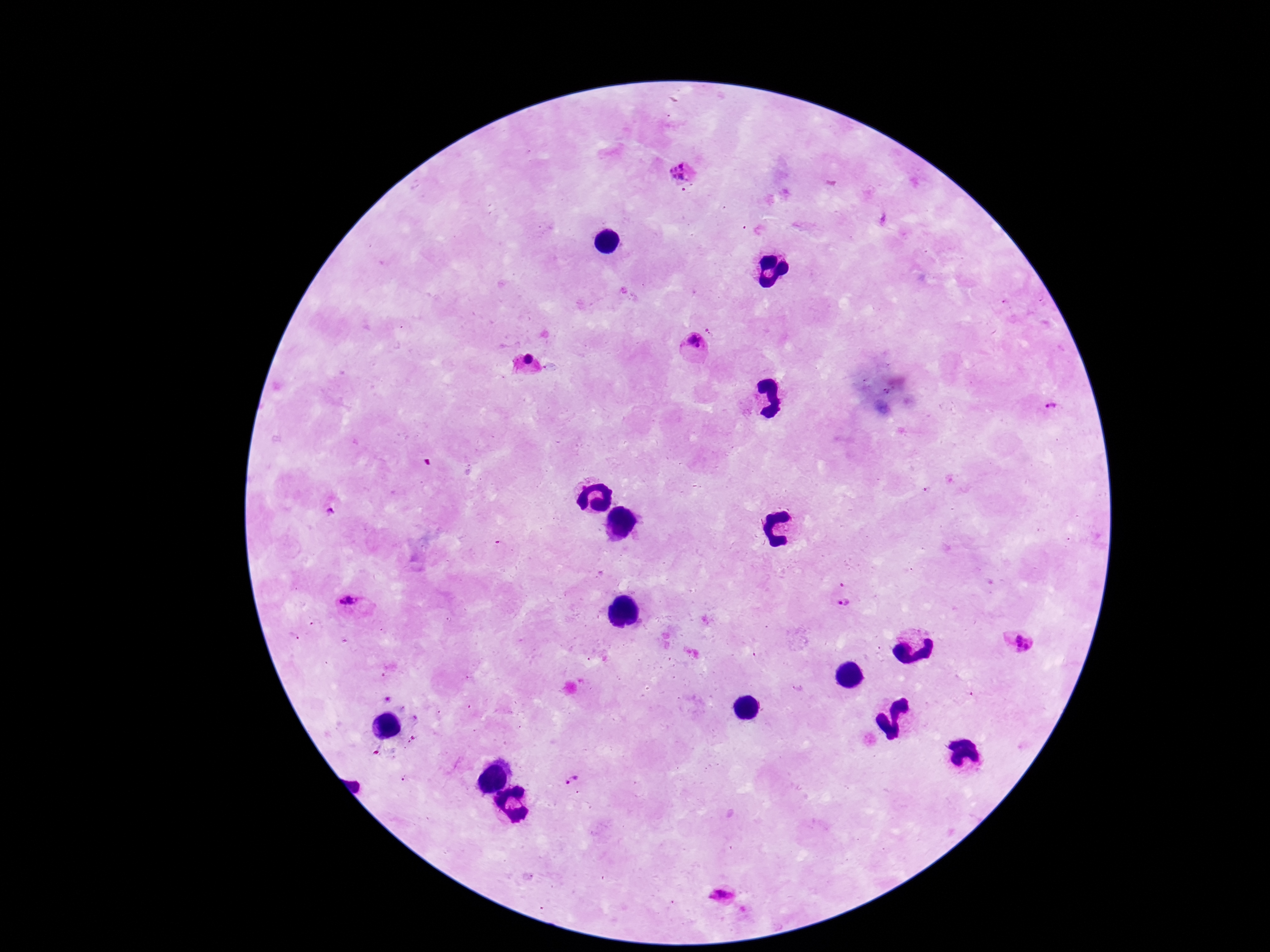
Approximate centers as (x, y) in pixels.
Summary:
  - Plasmodium parasite locations: (683, 174), (692, 346), (526, 366), (1051, 407), (333, 510), (842, 601), (353, 607), (1021, 642), (572, 782), (724, 896)
  - Patient malaria status: positive
  - Stain: Giemsa
  - Image size: 1270×952 pixels
  - Field of view: single
  - Capture: smartphone camera through the microscope eyepiece
  - Preparation: thick blood film
  - Magnification: 100x